Report the malaria status of this cell.
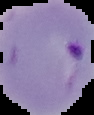
It is parasitized.

{
  "image_type": "segmented cell region on a black background",
  "image_size": "94×115 pixels",
  "preparation": "thin blood film"
}